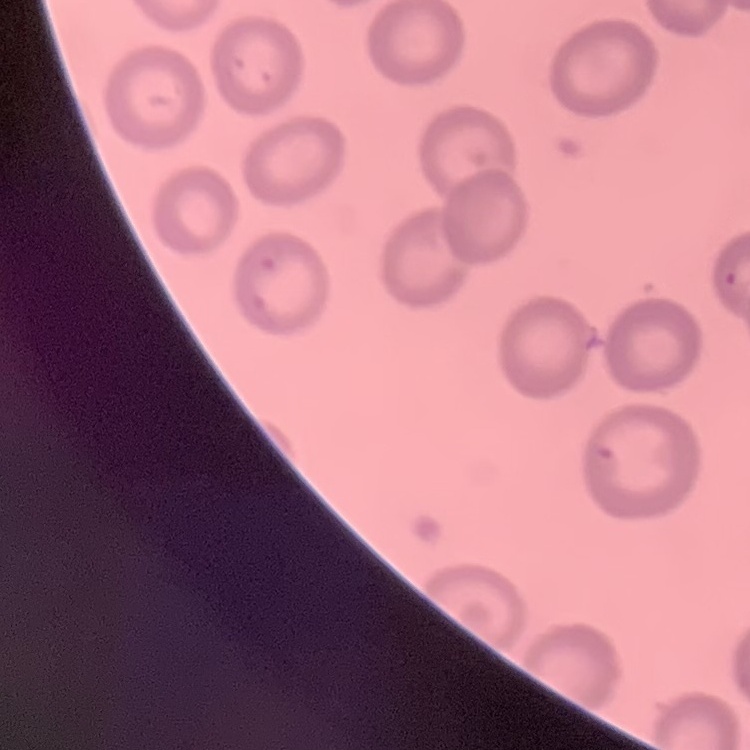

Summary:
  - Erythrocyte morphology: no rouleaux formation
  - Preparation: thin blood film
  - Stain: Field's or Giemsa
  - Image type: one tile cut from a larger photomicrograph